Locate every Plasmodium parasite.
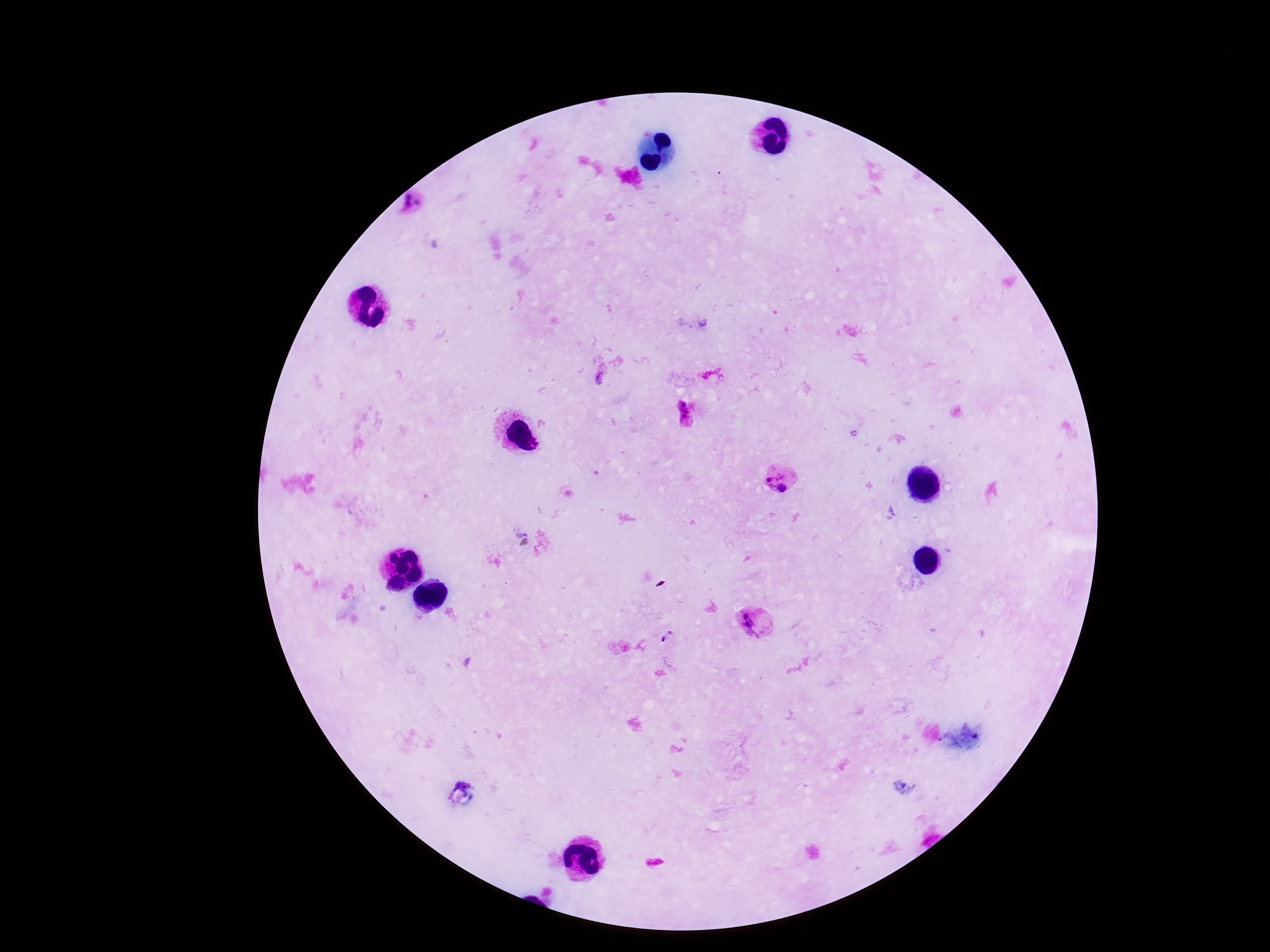

Approximate centers as {x, y} in pixels.
Plasmodium parasites: {415, 208}, {686, 413}, {778, 479}, {757, 622}, {663, 640}.

{
  "preparation": "thick blood film",
  "stain": "Giemsa",
  "magnification": "100x",
  "field_of_view": "one from this slide",
  "image_size": "1270×952 pixels",
  "capture": "smartphone camera through the microscope eyepiece",
  "patient_malaria_status": "positive"
}